Outline each Plasmodium falciparum-infected red blood cell.
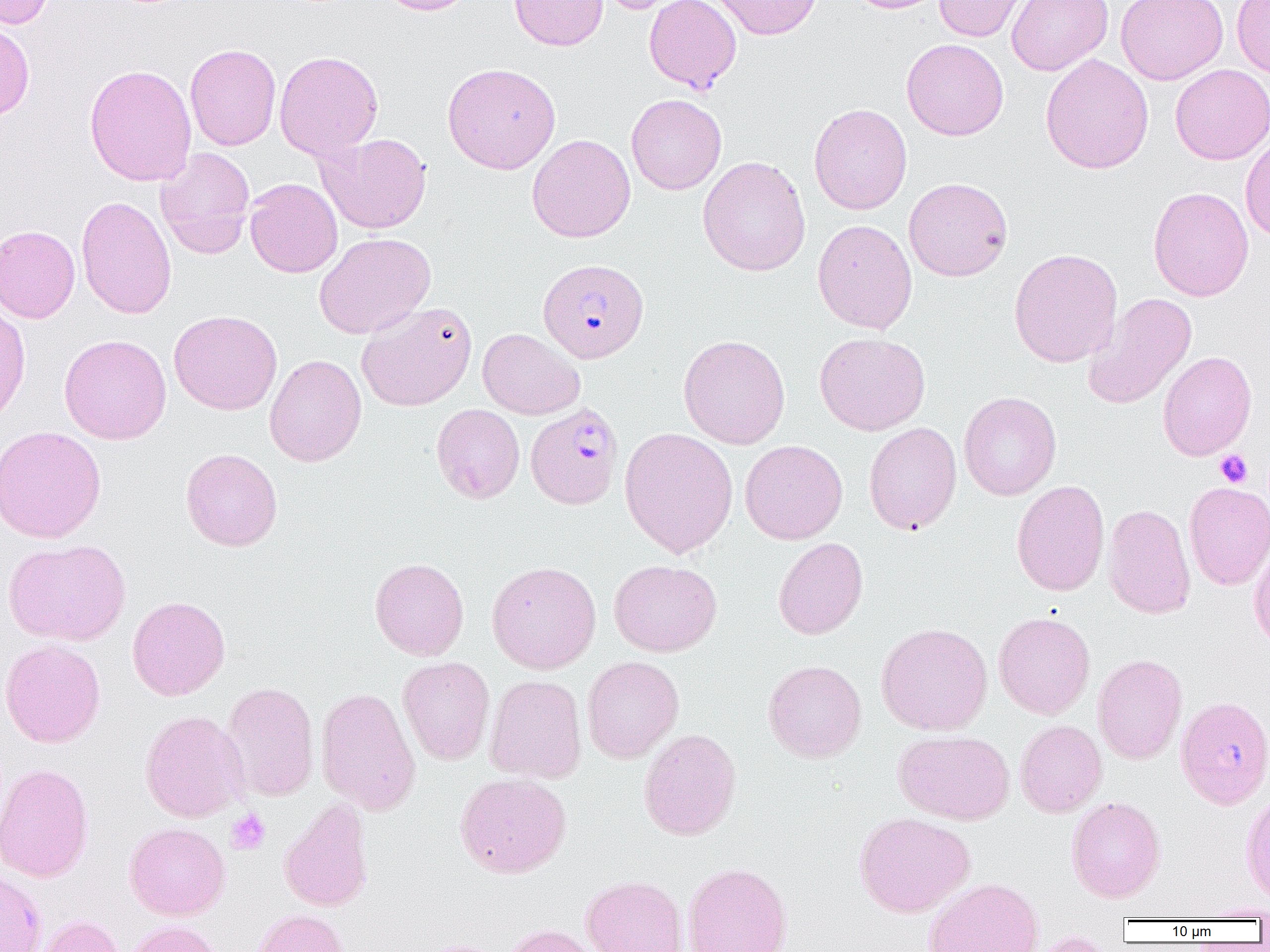

Approximate bounding boxes as [x1, y1, x2, y2] in pixels.
Plasmodium falciparum-infected red blood cells: [538, 258, 648, 363], [525, 402, 623, 508], [1175, 695, 1270, 809].

Platelet locations: [1215, 449, 1253, 488], [226, 809, 270, 854]. Uninfected red blood cell locations: [1, 0, 56, 29], [379, 0, 476, 15], [510, 0, 608, 51], [595, 0, 684, 14], [644, 0, 742, 93], [710, 0, 823, 40], [846, 0, 947, 14], [934, 0, 1030, 41], [1007, 0, 1113, 76], [1116, 0, 1228, 85], [1231, 0, 1270, 78], [0, 21, 34, 121], [901, 38, 1009, 141], [184, 43, 281, 151], [274, 51, 383, 160], [1040, 54, 1154, 174], [442, 62, 561, 174], [84, 64, 197, 186], [1169, 64, 1270, 165], [626, 93, 727, 195], [808, 103, 912, 215], [317, 132, 432, 234], [527, 134, 635, 242], [1240, 134, 1270, 244], [156, 147, 255, 259], [698, 156, 811, 276], [904, 177, 1013, 281], [244, 178, 343, 278], [1148, 186, 1254, 301], [75, 195, 177, 319], [813, 219, 917, 334], [0, 225, 80, 323], [314, 233, 436, 339], [1009, 248, 1123, 367], [1083, 293, 1197, 410], [356, 301, 478, 411], [0, 303, 31, 424], [168, 310, 282, 415], [477, 328, 585, 420], [814, 331, 930, 435], [59, 334, 172, 444], [678, 334, 790, 449], [1158, 350, 1256, 461], [264, 354, 366, 467], [958, 391, 1061, 500], [431, 404, 525, 503], [863, 422, 962, 535], [0, 425, 107, 543], [620, 427, 738, 558], [740, 440, 848, 544], [180, 448, 283, 551], [1011, 479, 1109, 596], [1184, 481, 1270, 590], [1103, 503, 1196, 620], [773, 537, 868, 639], [1249, 537, 1270, 651], [2, 539, 131, 645], [370, 557, 469, 660], [609, 559, 722, 656], [487, 561, 601, 673], [127, 596, 230, 700], [993, 611, 1095, 719], [876, 622, 992, 735], [1, 639, 106, 748], [1092, 653, 1188, 764], [398, 656, 495, 766], [581, 656, 684, 763], [764, 660, 867, 763], [484, 674, 587, 784], [220, 681, 319, 802], [315, 687, 420, 814], [139, 710, 249, 822], [1015, 719, 1106, 817], [638, 728, 741, 840], [893, 730, 1015, 825], [0, 763, 94, 883], [455, 773, 571, 878], [1240, 790, 1270, 906], [1066, 796, 1166, 903], [279, 800, 374, 912], [854, 812, 975, 917], [124, 822, 230, 920], [682, 862, 793, 952], [0, 868, 46, 952], [581, 875, 687, 952], [922, 877, 1044, 952], [1194, 901, 1270, 920], [252, 909, 348, 952], [34, 915, 125, 952], [124, 921, 225, 952], [501, 924, 603, 952], [1027, 932, 1114, 952], [413, 940, 506, 952]. Slide-level diagnosis: Plasmodium falciparum. Thin blood smear. Light microscopy. 1000x magnification. Single field of view. Image is 1270×952 pixels.